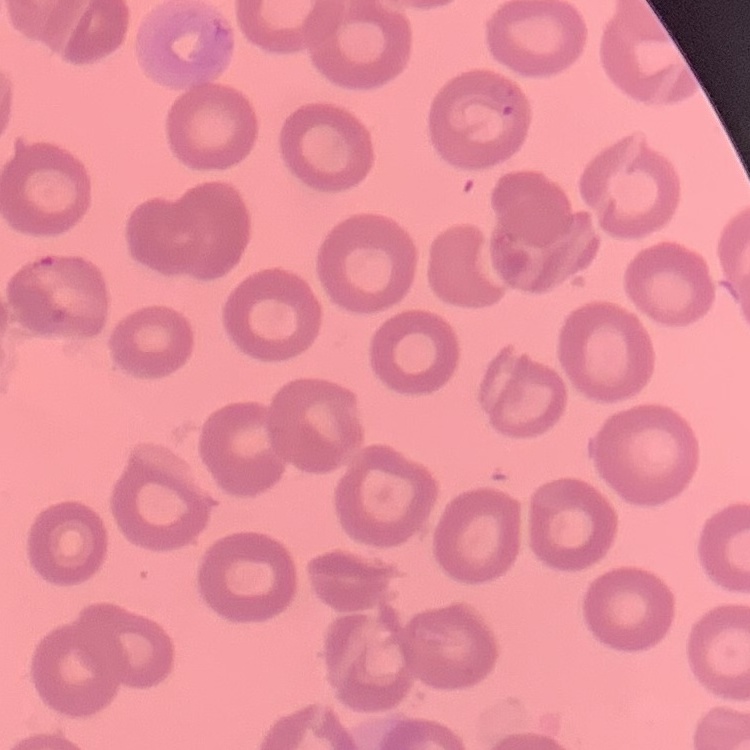
red blood cell morphology = no rouleaux formation
preparation = thin blood smear
image type = square crop of a larger photomicrograph
stain = Field's or Giemsa